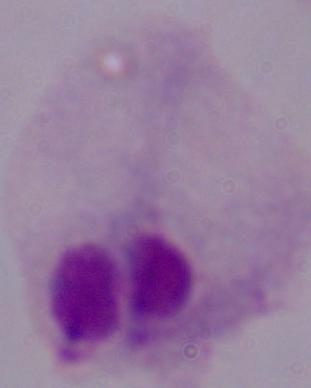

Summary:
  - Modality: micrograph
  - Identification: trichomonad
  - Magnification: 1000x